Assess this cell for malaria.
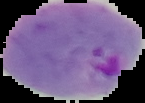

It is parasitized.

{
  "image_type": "segmented cell region with the area outside set to black",
  "preparation": "thin blood film",
  "image_size": "145×103 pixels"
}